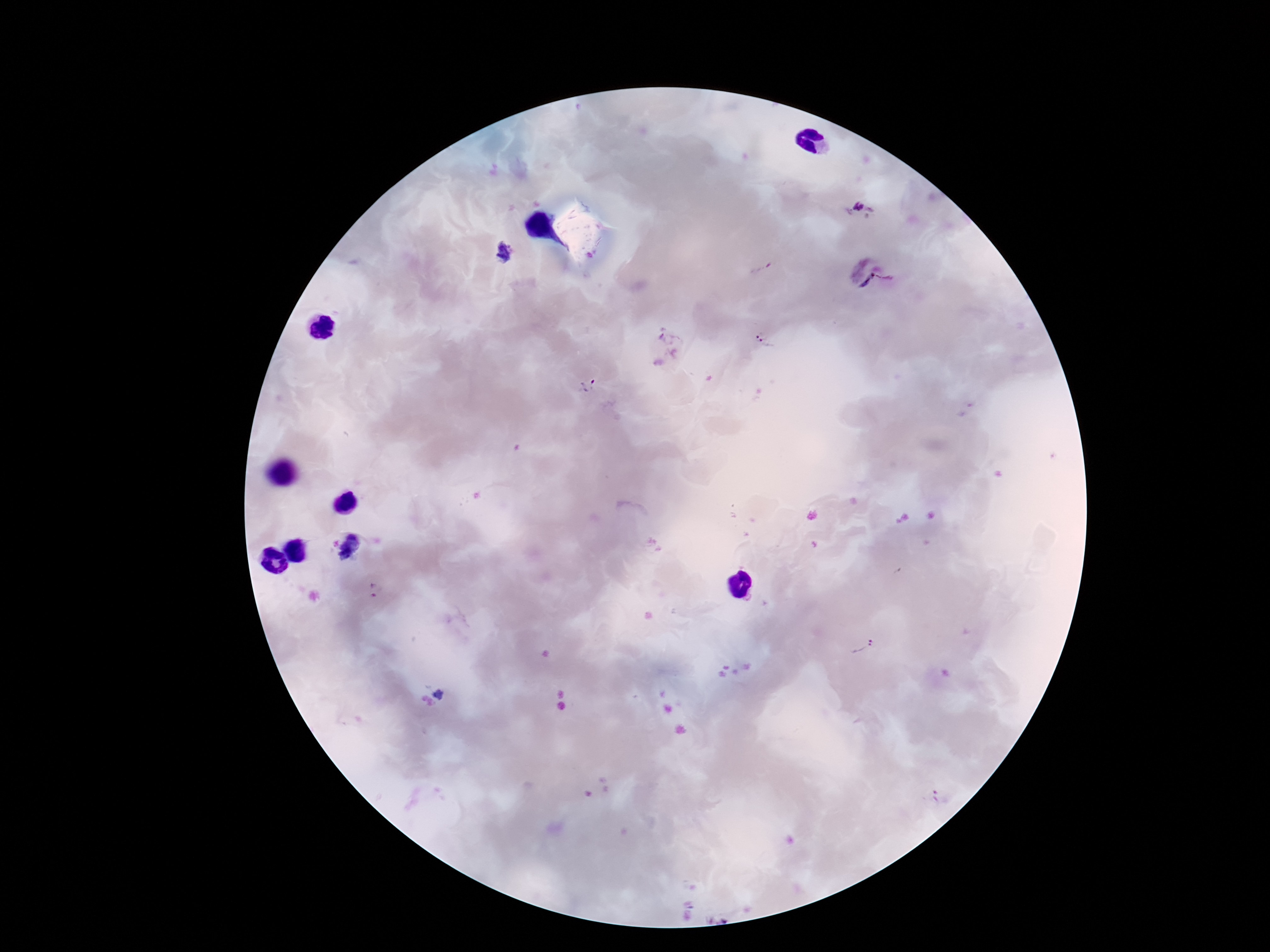 Approximate object centers, in pixels from the top-left corner. Plasmodium parasite locations: (x=859, y=207), (x=504, y=252), (x=760, y=265), (x=855, y=266), (x=872, y=274), (x=885, y=276), (x=866, y=282), (x=661, y=338), (x=764, y=339), (x=657, y=364), (x=587, y=385), (x=375, y=592), (x=859, y=646), (x=439, y=694), (x=936, y=797). 100x magnification. Image is 1270×952 pixels. Single field of view. Smartphone photograph taken through the microscope eyepiece. Patient malaria status: infected. Giemsa-stained preparation. Thick peripheral-blood smear.